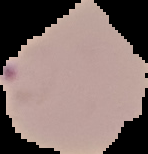 Image is 148×154 pixels. Cell region segmented out of the field of view; the surrounding area is masked to black. Malaria status: parasitized. From a thin blood smear.